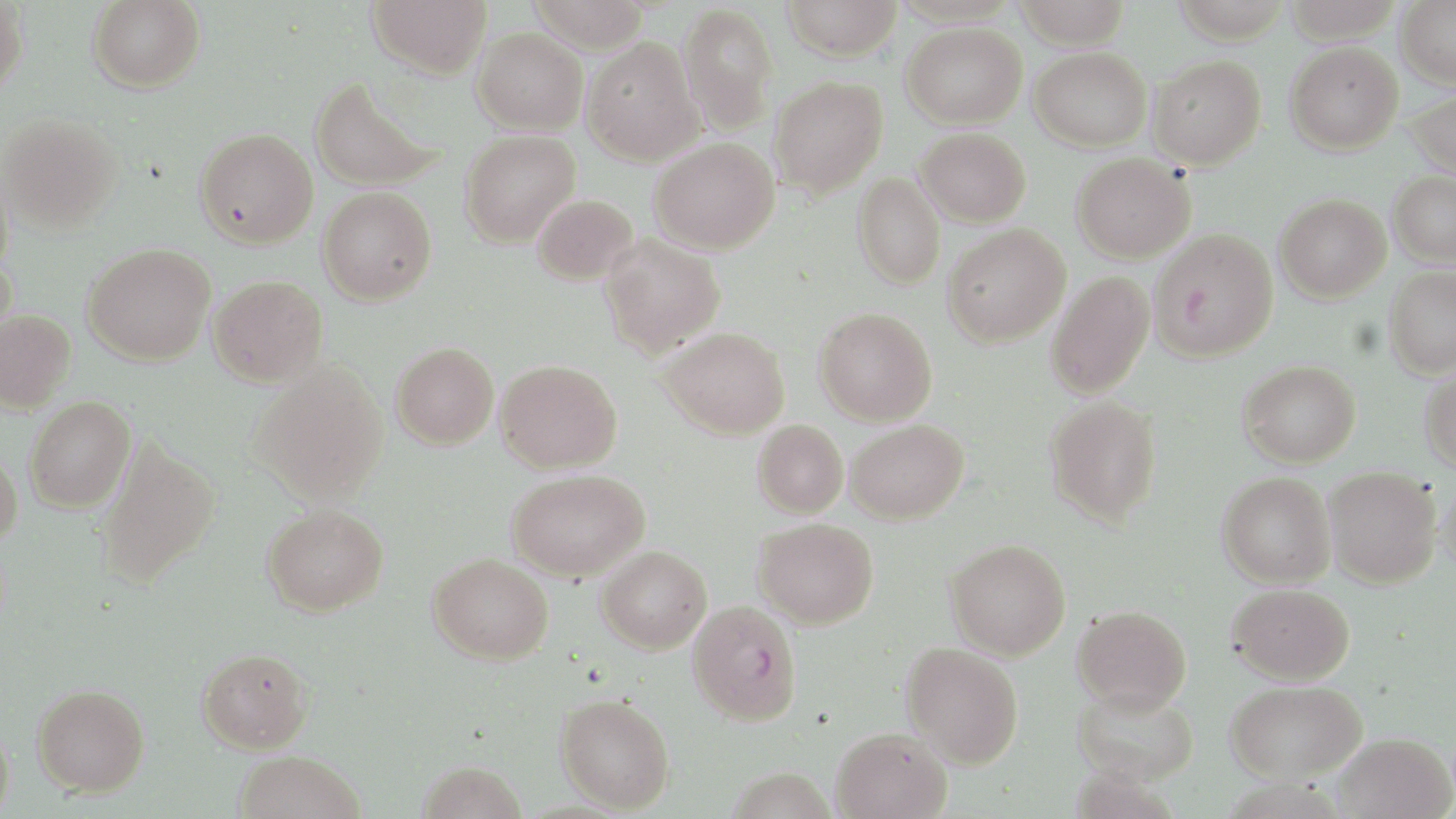

slide-level diagnosis = Plasmodium falciparum
uninfected red blood cell locations = approximate bounding boxes as named x1/y1/x2/y2 corners in pixels: (x1=87, y1=0, x2=205, y2=93), (x1=368, y1=0, x2=492, y2=79), (x1=525, y1=0, x2=651, y2=54), (x1=780, y1=0, x2=903, y2=61), (x1=1014, y1=0, x2=1131, y2=49), (x1=1172, y1=0, x2=1292, y2=43), (x1=1282, y1=0, x2=1403, y2=42), (x1=1396, y1=0, x2=1456, y2=88), (x1=0, y1=1, x2=29, y2=94), (x1=678, y1=2, x2=778, y2=135), (x1=902, y1=22, x2=1027, y2=129), (x1=472, y1=27, x2=588, y2=135), (x1=581, y1=35, x2=704, y2=166), (x1=1285, y1=42, x2=1403, y2=154), (x1=1030, y1=47, x2=1152, y2=151), (x1=1148, y1=56, x2=1266, y2=169), (x1=309, y1=75, x2=444, y2=193), (x1=769, y1=76, x2=888, y2=199), (x1=1406, y1=89, x2=1456, y2=180), (x1=0, y1=113, x2=122, y2=233), (x1=194, y1=127, x2=318, y2=250), (x1=916, y1=127, x2=1031, y2=227), (x1=459, y1=129, x2=581, y2=247), (x1=650, y1=137, x2=779, y2=254), (x1=1071, y1=153, x2=1195, y2=263), (x1=0, y1=162, x2=14, y2=284), (x1=1388, y1=171, x2=1456, y2=268), (x1=853, y1=172, x2=945, y2=290), (x1=318, y1=186, x2=437, y2=305), (x1=533, y1=193, x2=638, y2=285), (x1=1275, y1=193, x2=1391, y2=302), (x1=943, y1=224, x2=1070, y2=347), (x1=1149, y1=227, x2=1279, y2=362), (x1=599, y1=235, x2=726, y2=357), (x1=83, y1=243, x2=216, y2=367), (x1=1, y1=253, x2=18, y2=358), (x1=1384, y1=267, x2=1456, y2=379), (x1=1046, y1=272, x2=1154, y2=400), (x1=208, y1=275, x2=328, y2=387), (x1=814, y1=307, x2=937, y2=426), (x1=0, y1=309, x2=76, y2=412), (x1=659, y1=327, x2=790, y2=439), (x1=391, y1=341, x2=498, y2=450), (x1=495, y1=359, x2=622, y2=473), (x1=1238, y1=360, x2=1361, y2=468), (x1=251, y1=362, x2=389, y2=505), (x1=1420, y1=365, x2=1456, y2=473), (x1=24, y1=396, x2=136, y2=513), (x1=1043, y1=396, x2=1162, y2=526), (x1=846, y1=419, x2=969, y2=524), (x1=753, y1=420, x2=848, y2=517), (x1=94, y1=435, x2=221, y2=588), (x1=0, y1=445, x2=23, y2=548), (x1=1324, y1=466, x2=1441, y2=589), (x1=506, y1=469, x2=649, y2=580), (x1=1217, y1=471, x2=1335, y2=589), (x1=1438, y1=471, x2=1456, y2=579), (x1=262, y1=503, x2=388, y2=617), (x1=753, y1=518, x2=879, y2=629), (x1=945, y1=539, x2=1071, y2=660), (x1=597, y1=545, x2=712, y2=653), (x1=428, y1=552, x2=554, y2=664), (x1=1227, y1=583, x2=1355, y2=685), (x1=1072, y1=604, x2=1192, y2=713), (x1=900, y1=642, x2=1023, y2=768), (x1=197, y1=647, x2=314, y2=754), (x1=1226, y1=680, x2=1367, y2=783), (x1=31, y1=683, x2=150, y2=797), (x1=1073, y1=686, x2=1199, y2=787), (x1=555, y1=692, x2=676, y2=813), (x1=1, y1=720, x2=14, y2=819), (x1=830, y1=727, x2=952, y2=819), (x1=1333, y1=732, x2=1455, y2=819), (x1=233, y1=750, x2=366, y2=819), (x1=417, y1=759, x2=528, y2=819)
magnification = 1000x
field of view = single
Plasmodium falciparum-infected red blood cell locations = approximate bounding boxes as named x1/y1/x2/y2 corners in pixels: (x1=688, y1=600, x2=802, y2=725)
modality = light microscopy
stain = May-Grünwald-Giemsa
image size = 1456×819 pixels
preparation = thin blood film